Report the malaria status of this cell.
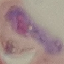

Parasitized.

{
  "preparation": "thin smear",
  "image_type": "cell patch, automatically extracted from a larger field of view and resized to 64 × 64 pixels",
  "capture": "smartphone camera at the microscope eyepiece",
  "stain": "Giemsa"
}